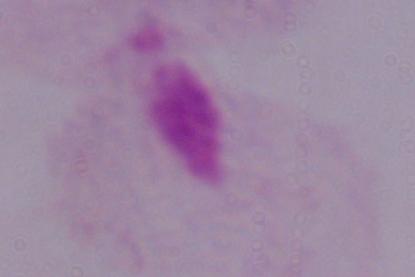

modality = micrograph
identification = trichomonad
magnification = 1000x